Give the extent of all uninfected red blood cells.
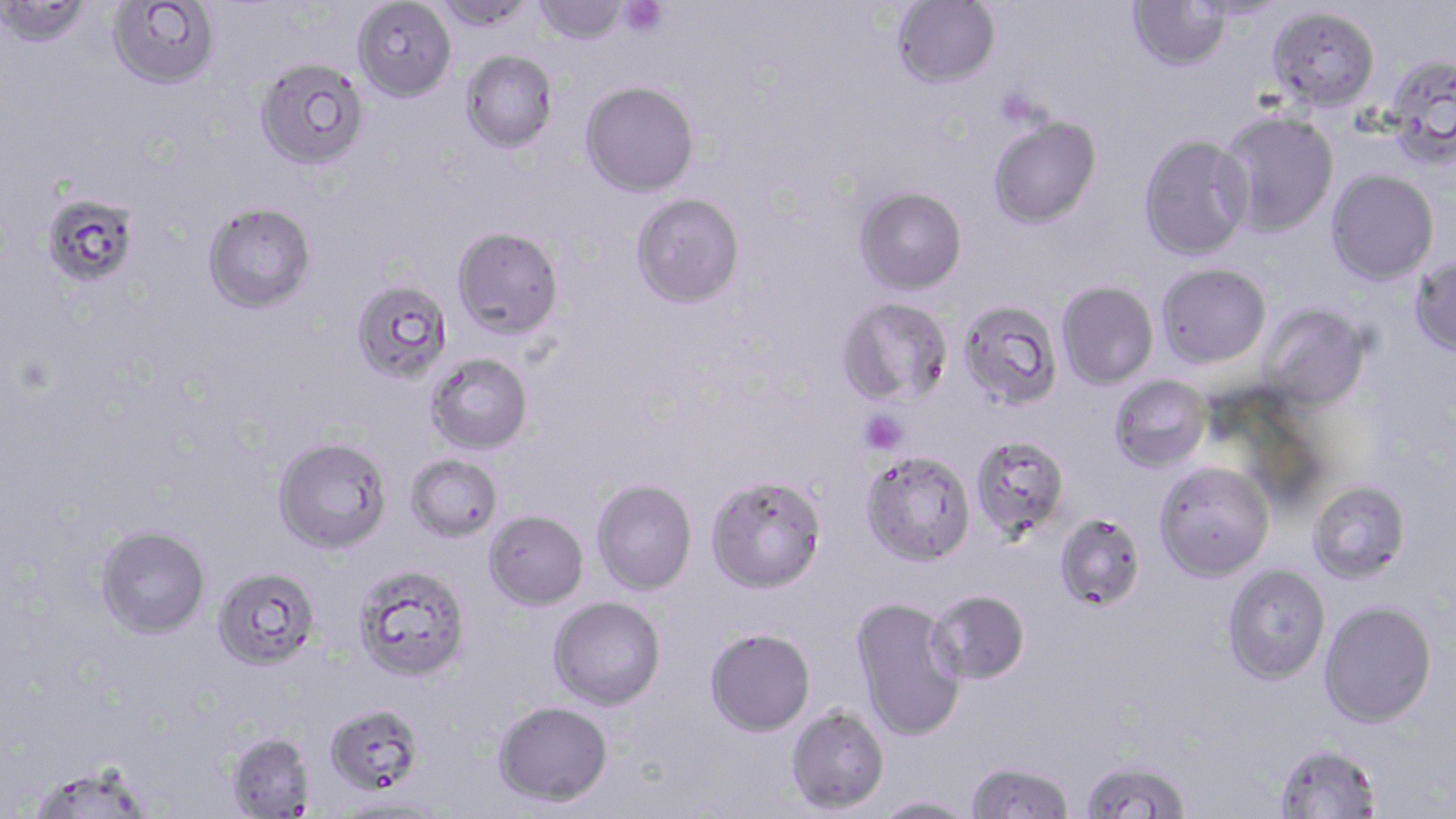
Approximate bounding boxes as (x1,y1)-(x2,y2) corner pairs in pixels.
Uninfected red blood cells: (108,0)-(220,89), (432,0)-(539,31), (534,0)-(629,45), (892,0)-(1000,88), (1128,0)-(1229,71), (0,1)-(92,46), (353,1)-(457,102), (1267,6)-(1380,111), (461,49)-(558,153), (1383,52)-(1456,166), (255,57)-(369,170), (580,81)-(699,197), (1217,110)-(1339,237), (987,116)-(1102,229), (1138,135)-(1253,260), (1326,169)-(1439,285), (855,186)-(968,295), (42,192)-(140,289), (631,193)-(745,308), (203,202)-(317,313), (452,226)-(564,338), (1411,256)-(1456,356), (1156,263)-(1271,368), (1056,281)-(1158,390), (355,285)-(446,377), (836,297)-(953,407), (959,301)-(1062,409), (1260,304)-(1371,412), (426,353)-(534,455), (1108,375)-(1212,474), (969,434)-(1071,539), (273,436)-(392,554), (860,450)-(976,566), (406,453)-(503,543), (1154,461)-(1274,581), (705,474)-(827,594), (591,478)-(698,595), (1308,480)-(1411,584), (484,510)-(589,610), (1054,512)-(1147,611), (96,525)-(211,638), (354,563)-(470,682), (1222,564)-(1331,684), (212,566)-(320,671), (928,588)-(1031,684), (548,596)-(666,709), (850,597)-(967,741), (1319,600)-(1438,728), (704,627)-(816,736), (493,700)-(613,807), (325,703)-(426,797), (786,705)-(890,814), (227,732)-(314,817), (1273,743)-(1382,818), (1078,760)-(1193,818), (964,762)-(1076,819), (27,763)-(155,818), (337,796)-(449,818), (872,796)-(979,818).

slide_level_diagnosis: Plasmodium falciparum
magnification: 1000x
modality: optical microscopy
stain: May-Grünwald-Giemsa
platelet_locations: 'approximate bounding boxes as (x1,y1)-(x2,y2) corner pairs in pixels: (619,0)-(668,37), (995,87)-(1042,129), (859,409)-(909,454)'
preparation: thin blood film
image_size: 1456×819 pixels
field_of_view: single